Assess this cell for malaria.
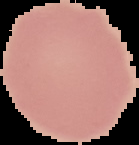

It is uninfected.

image_size: 139×145 pixels
image_type: cell region segmented out of the field of view; surrounding area masked to black
preparation: thin blood smear